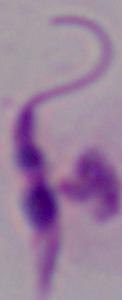
{
  "modality": "photomicrograph",
  "identification": "Leishmania",
  "magnification": "1000x"
}